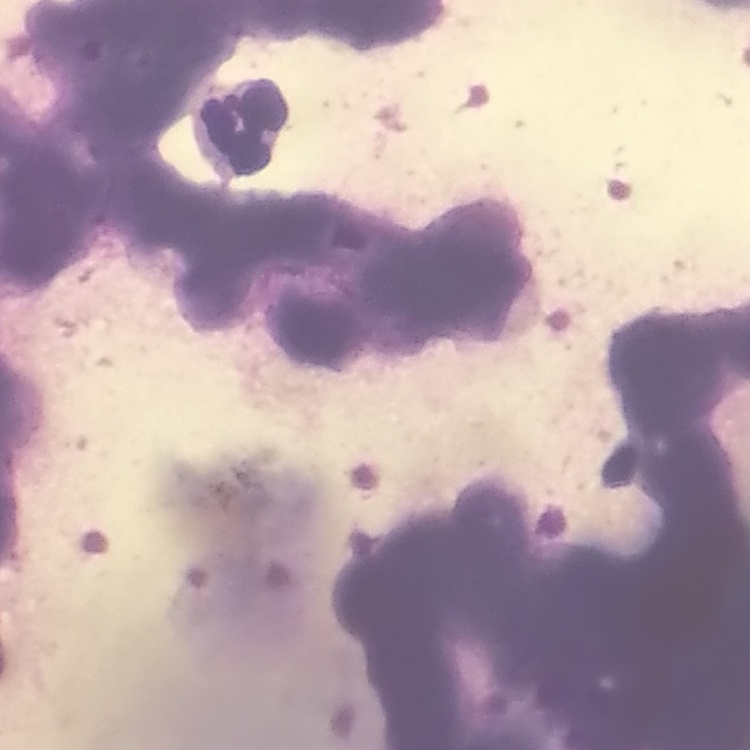
Summary:
  - Erythrocyte morphology: rouleaux formation
  - Stain: Field's or Giemsa
  - Preparation: thin blood smear
  - Image type: square crop of a larger photomicrograph